Describe the morphology of the red blood cells.
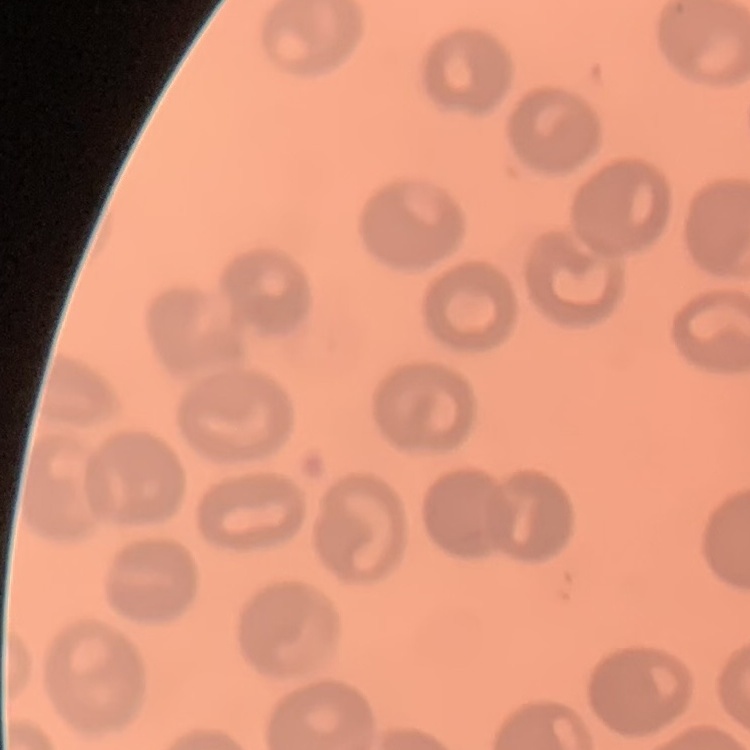

No rouleaux formation.

Summary:
  - Stain: Field's or Giemsa
  - Image type: one tile cut from a larger photomicrograph
  - Preparation: thin peripheral smear